Classify this cell by malaria status.
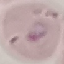

Parasitized.

Summary:
  - Preparation: thin blood smear
  - Image type: automatically extracted cell patch, resized to 64 × 64 pixels
  - Stain: Giemsa
  - Capture: smartphone camera at the microscope eyepiece